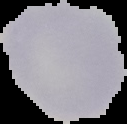 Image is 127×124 pixels. From a thin blood film. Malaria status: uninfected. Cell region segmented out of the field of view; the surrounding area is masked to black.